Report the malaria status of this cell.
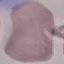

Uninfected.

Photographed with a smartphone camera at the microscope eyepiece. Giemsa-stained preparation. Thin smear of blood. Cell patch, automatically extracted from a larger field of view and resized to 64 × 64 pixels.